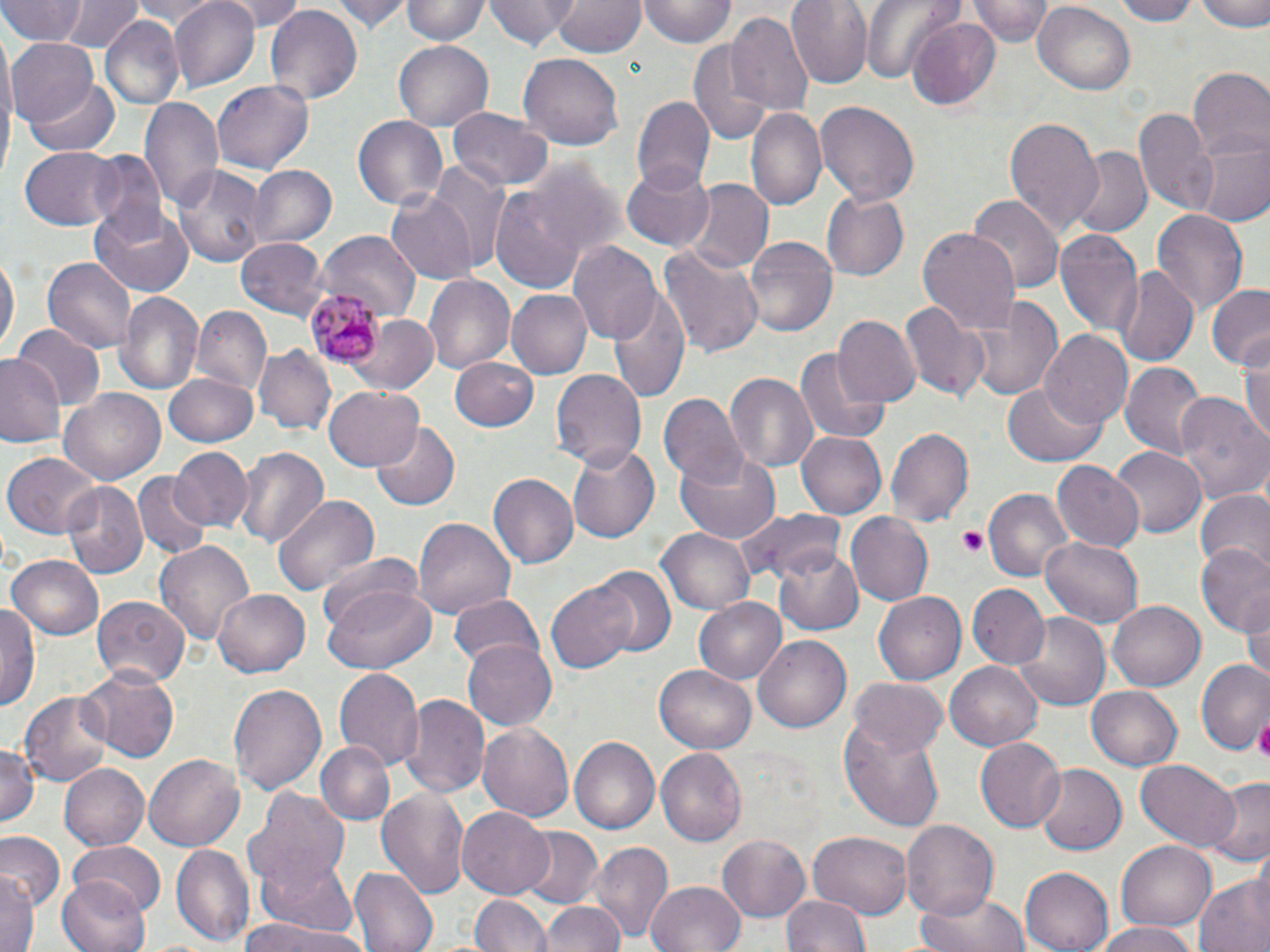
slide_level_diagnosis: Plasmodium malariae
image_size: 1270×952 pixels
modality: optical microscopy
field_of_view: one of a larger specimen
stain: May-Grünwald-Giemsa
uninfected_red_blood_cell_locations: 'approximate bounding boxes as (x1, y1, x2, y2) in pixels: (62, 0, 140, 51), (127, 0, 227, 26), (170, 0, 258, 90), (222, 0, 308, 32), (333, 0, 408, 34), (401, 0, 487, 46), (486, 0, 578, 51), (550, 0, 645, 58), (641, 0, 734, 46), (788, 0, 874, 88), (861, 0, 957, 84), (969, 0, 1052, 45), (1110, 0, 1198, 24), (1197, 0, 1270, 31), (0, 2, 87, 46), (1032, 3, 1136, 95), (263, 6, 363, 106), (727, 12, 815, 116), (100, 16, 186, 110), (909, 17, 1004, 108), (687, 36, 773, 146), (7, 37, 102, 131), (392, 38, 497, 131), (518, 52, 626, 149), (1187, 71, 1269, 163), (27, 75, 120, 154), (212, 79, 314, 171), (631, 96, 715, 194), (139, 98, 223, 212), (815, 101, 919, 207), (746, 106, 827, 213), (1132, 106, 1213, 209), (447, 108, 554, 192), (353, 115, 448, 210), (1004, 115, 1104, 235), (1190, 136, 1269, 228), (18, 146, 123, 230), (1067, 147, 1151, 237), (87, 150, 166, 239), (426, 160, 514, 276), (171, 163, 267, 268), (622, 163, 713, 250), (247, 165, 335, 248), (679, 181, 773, 275), (489, 185, 589, 290), (386, 188, 480, 283), (819, 190, 909, 281), (969, 193, 1063, 294), (91, 207, 193, 296), (1151, 210, 1248, 318), (1054, 225, 1142, 340), (917, 227, 1022, 333), (318, 233, 422, 319), (745, 234, 838, 337), (236, 236, 330, 318), (569, 241, 662, 343), (659, 247, 764, 358), (0, 249, 17, 358), (42, 257, 135, 354), (1114, 265, 1198, 367), (423, 273, 516, 375), (1208, 285, 1270, 369), (610, 286, 689, 399), (115, 290, 203, 395), (506, 290, 591, 378), (957, 291, 1067, 403), (898, 298, 988, 404), (189, 305, 271, 396), (835, 315, 921, 409), (347, 317, 436, 393), (11, 326, 103, 414), (1041, 330, 1133, 429), (1238, 340, 1270, 447), (255, 344, 336, 437), (797, 348, 891, 443), (0, 355, 66, 450), (450, 356, 541, 432), (1119, 361, 1207, 458), (551, 368, 646, 469), (165, 372, 261, 447), (723, 372, 819, 476), (1003, 380, 1105, 465), (323, 386, 423, 471), (61, 388, 164, 483), (1172, 391, 1269, 505), (660, 392, 748, 493), (371, 423, 461, 513), (886, 426, 974, 526), (796, 433, 887, 518), (565, 440, 661, 543), (232, 446, 329, 549), (1109, 447, 1205, 538), (172, 448, 252, 531), (676, 448, 781, 542), (2, 453, 100, 538), (1051, 461, 1143, 555), (133, 472, 212, 558), (487, 473, 579, 570), (59, 482, 147, 579), (984, 489, 1075, 582), (1194, 491, 1270, 575), (272, 493, 379, 594), (733, 507, 848, 586), (847, 512, 933, 606), (413, 517, 517, 619), (655, 528, 755, 615), (1040, 536, 1143, 630), (153, 540, 256, 648), (773, 542, 863, 634), (1195, 543, 1270, 634), (7, 554, 105, 640), (316, 555, 426, 642), (590, 566, 676, 657), (547, 581, 636, 672), (967, 583, 1049, 667), (324, 585, 437, 674), (212, 588, 312, 677), (875, 591, 969, 685), (448, 592, 545, 673), (92, 595, 190, 687), (1242, 595, 1270, 686), (693, 597, 788, 685), (1107, 600, 1206, 691), (0, 602, 40, 714), (1012, 612, 1113, 714), (754, 634, 850, 731), (463, 640, 557, 732), (1198, 661, 1270, 757), (946, 662, 1042, 750), (79, 664, 181, 760), (654, 664, 756, 755), (333, 667, 424, 771), (850, 677, 947, 759), (229, 681, 326, 798), (1086, 687, 1184, 771), (20, 688, 113, 785), (400, 693, 490, 797), (478, 721, 574, 824), (840, 723, 945, 830), (976, 737, 1065, 831), (568, 738, 658, 835), (318, 741, 393, 823), (0, 743, 41, 830), (657, 749, 747, 847), (146, 754, 243, 852), (1136, 760, 1240, 853), (59, 764, 148, 851), (1036, 766, 1129, 854), (1205, 778, 1270, 864), (245, 781, 356, 900), (376, 787, 468, 898), (457, 807, 555, 899), (901, 820, 998, 921), (517, 827, 604, 912), (0, 830, 64, 909), (717, 832, 812, 922), (808, 833, 914, 917), (1116, 839, 1217, 929), (588, 841, 673, 945), (70, 843, 165, 920), (171, 844, 254, 947), (350, 866, 438, 952), (1020, 867, 1114, 951), (0, 871, 39, 952), (58, 875, 152, 952), (1195, 876, 1270, 952), (255, 879, 368, 949), (648, 882, 746, 952), (916, 888, 1029, 952), (782, 894, 870, 952), (473, 895, 551, 952), (541, 899, 625, 952), (243, 914, 362, 952), (1088, 921, 1205, 952)'
magnification: 1000x
platelet_locations: 'approximate bounding boxes as (x1, y1, x2, y2) in pixels: (954, 528, 990, 556), (1254, 714, 1270, 765)'
preparation: thin blood smear
plasmodium_malariae_infected_red_blood_cell_locations: 'approximate bounding boxes as (x1, y1, x2, y2) in pixels: (307, 289, 387, 365)'